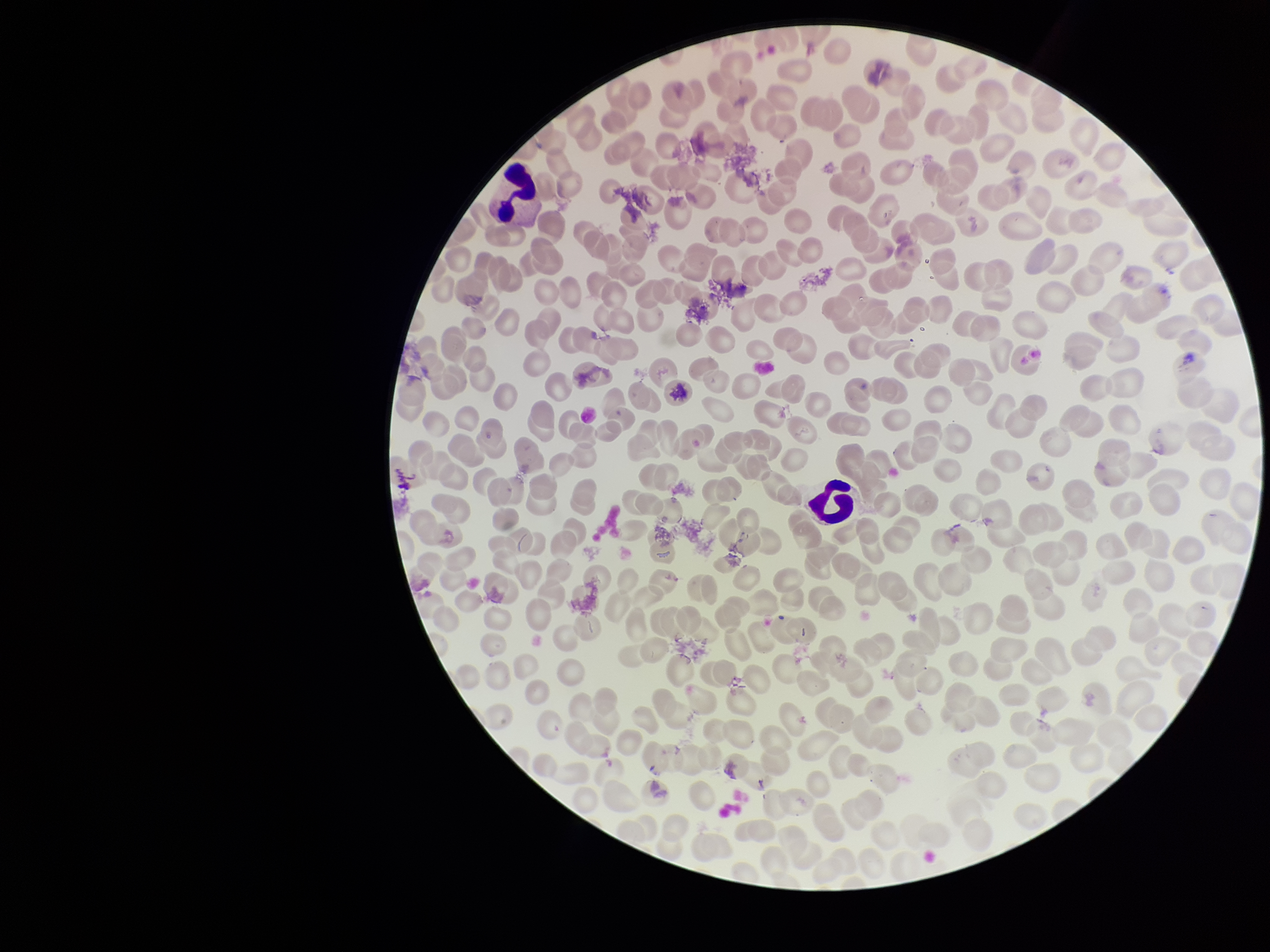

red blood cell count = 176
parasitized red blood cells = none identified
preparation = thin blood smear
stain = Giemsa
parasitized red blood cell count = 0
capture = smartphone photograph through the microscope eyepiece
patient malaria status = negative
field of view = single
image size = 1270×952 pixels